Assess the morphology of the red blood cells.
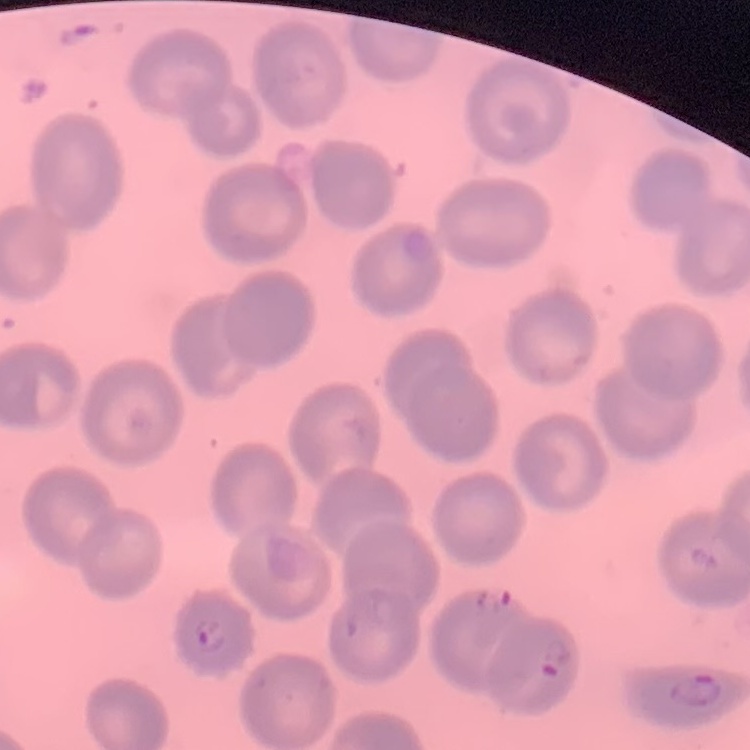
They show no rouleaux formation.

Thin peripheral smear. Stained with either Field's or Giemsa. Square crop of a larger photomicrograph.